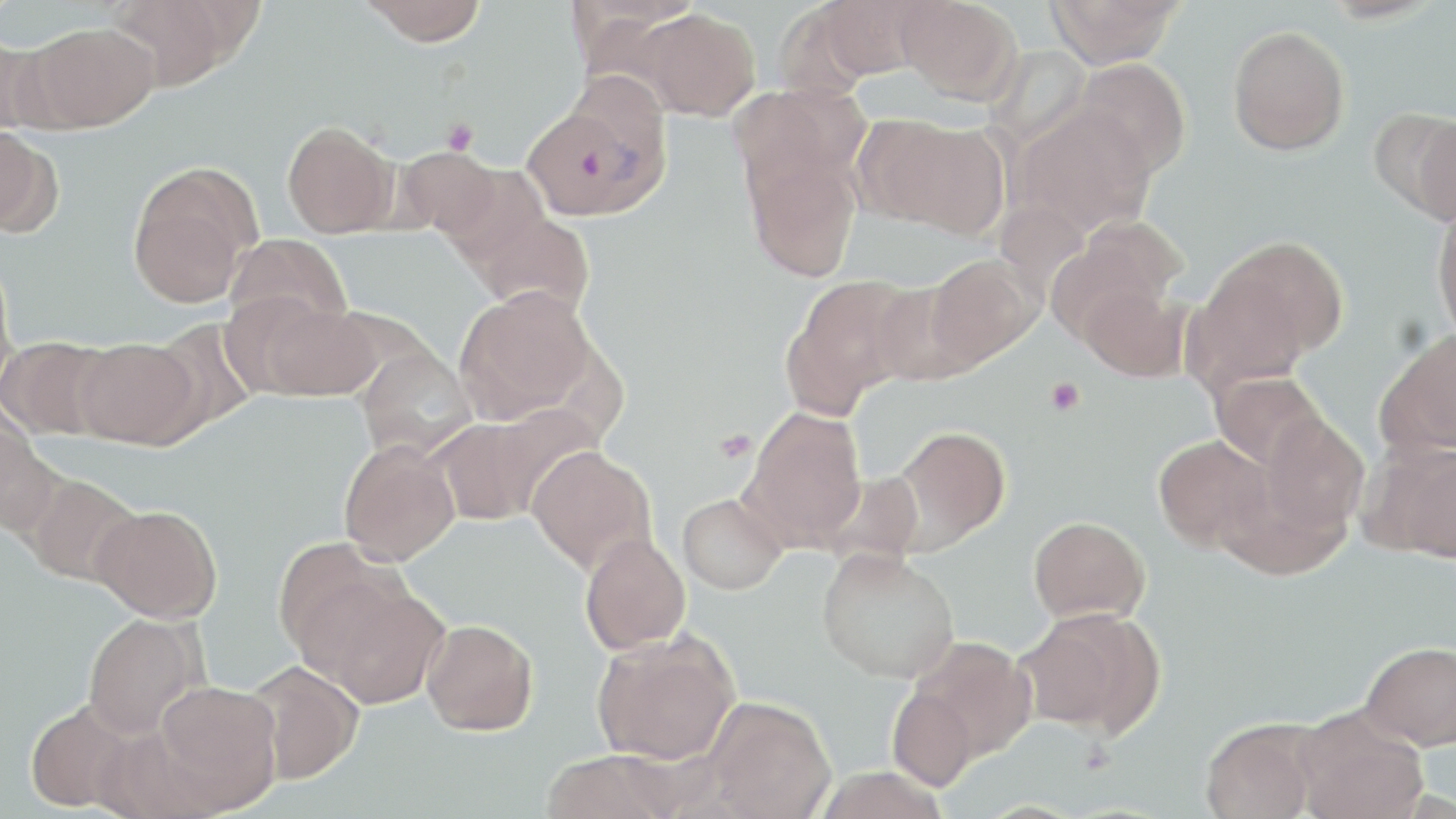
slide-level diagnosis = Plasmodium vivax
magnification = 1000x
image size = 1456×819 pixels
platelet locations = approximate bounding boxes as (x1,y1)-(x2,y2) corner pairs in pixels: (441,117)-(479,155), (1044,378)-(1086,416), (713,429)-(757,463)
preparation = thin blood smear
field of view = one of a larger specimen
stain = May-Grünwald-Giemsa
uninfected red blood cell locations = approximate bounding boxes as (x1,y1)-(x2,y2) corner pairs in pixels: (107,0)-(241,92), (816,0)-(932,79), (894,0)-(1021,102), (1046,0)-(1183,68), (359,1)-(489,46), (771,3)-(881,101), (638,8)-(761,121), (27,22)-(159,131), (1227,25)-(1349,156), (0,35)-(52,136), (983,45)-(1092,150), (1074,59)-(1192,177), (728,82)-(867,197), (1014,107)-(1156,236), (1403,111)-(1456,228), (868,117)-(1009,237), (282,120)-(399,238), (0,127)-(55,237), (391,146)-(505,240), (744,149)-(861,282), (437,163)-(551,266), (127,164)-(258,308), (1431,205)-(1456,343), (470,212)-(595,319), (1047,217)-(1187,340), (224,234)-(352,337), (1202,235)-(1348,373), (0,250)-(19,401), (924,254)-(1041,370), (784,273)-(923,412), (869,277)-(983,386), (1077,281)-(1190,381), (455,286)-(598,425), (249,298)-(381,402), (150,317)-(260,434), (1375,329)-(1456,458), (0,336)-(117,440), (74,336)-(202,449), (355,345)-(477,461), (1210,371)-(1328,474), (741,407)-(867,549), (428,408)-(583,525), (0,411)-(56,536), (1256,412)-(1370,539), (890,426)-(1011,554), (1152,435)-(1272,552), (338,439)-(460,566), (1374,441)-(1455,563), (526,445)-(657,575), (817,469)-(925,568), (20,472)-(143,586), (677,493)-(787,594), (91,504)-(222,623), (1028,515)-(1150,626), (579,532)-(691,655), (273,538)-(397,667), (817,548)-(959,684), (311,579)-(450,709), (1016,607)-(1164,736), (83,613)-(201,738), (421,618)-(538,736), (591,632)-(740,765), (911,636)-(1037,762), (1361,640)-(1456,750), (244,660)-(364,784), (152,681)-(283,811), (887,686)-(980,792), (705,696)-(836,819), (25,701)-(135,813), (1294,710)-(1430,819), (1199,718)-(1322,819), (541,750)-(680,819)
modality = optical microscopy
Plasmodium vivax-infected red blood cell locations = approximate bounding boxes as (x1,y1)-(x2,y2) corner pairs in pixels: (521,93)-(665,222)